Classify this cell by malaria status.
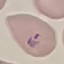
Parasitized.

capture = smartphone camera at the microscope eyepiece
stain = Giemsa
image type = automatically extracted cell patch, resized to 64 × 64 pixels
preparation = thin smear